Name the parasite shown.
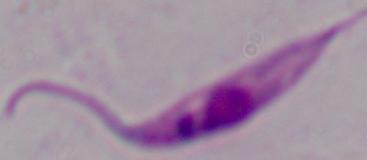

Leishmania.

1000x magnification. Micrograph.